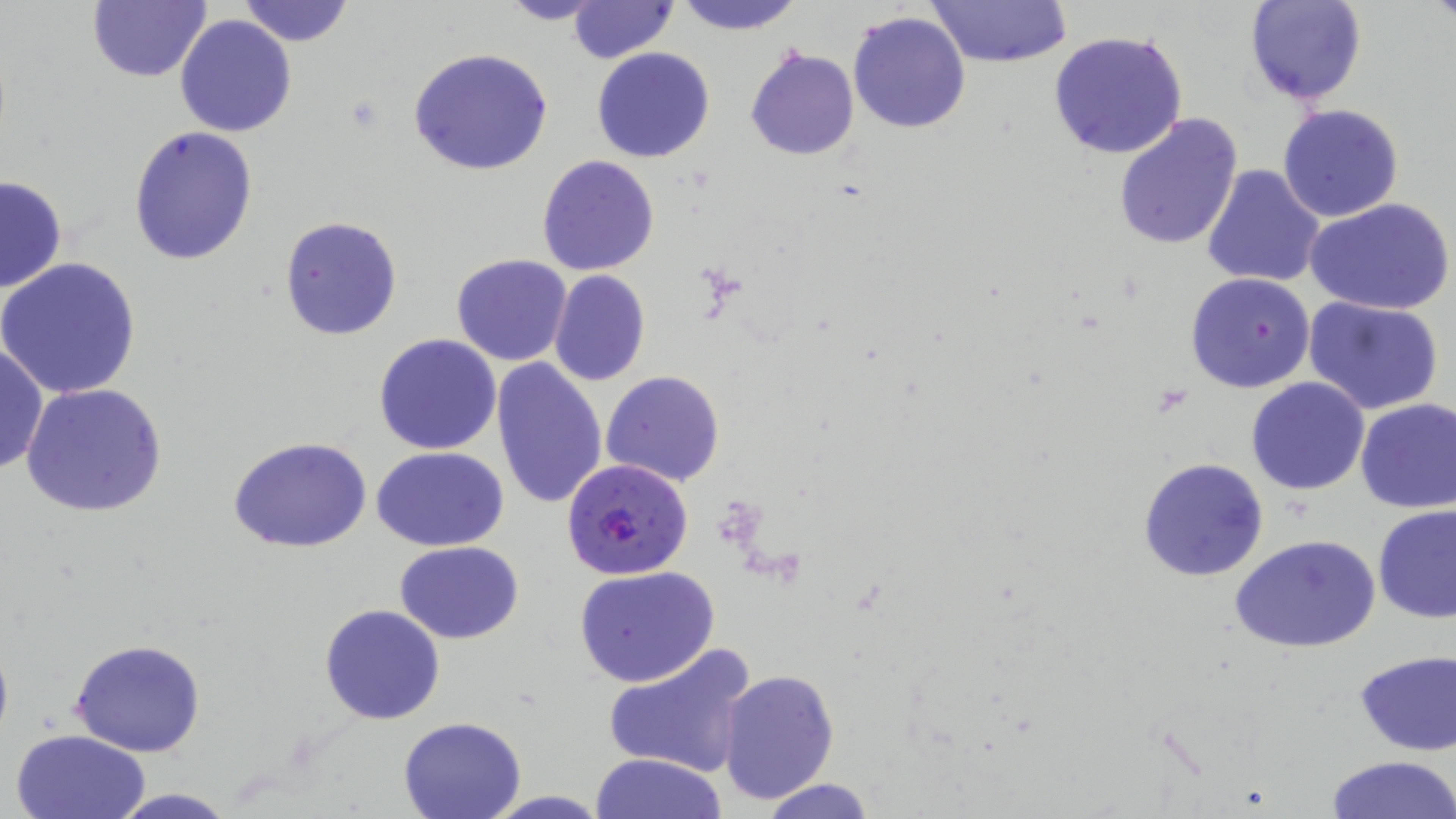

slide-level diagnosis = Plasmodium falciparum
field of view = one of a larger specimen
uninfected red blood cell locations = approximate bounding boxes as (x1,y1)-(x2,y2) corner pairs in pixels: (87,0)-(212,84), (236,0)-(356,48), (494,0)-(613,26), (670,0)-(804,35), (925,0)-(1072,69), (1244,0)-(1366,106), (570,1)-(676,61), (847,10)-(971,134), (174,14)-(298,137), (1047,29)-(1188,160), (407,47)-(553,176), (591,47)-(715,163), (745,48)-(859,161), (1277,104)-(1405,222), (1112,111)-(1242,252), (128,126)-(259,267), (537,155)-(659,276), (1201,164)-(1327,288), (0,174)-(67,295), (1306,198)-(1455,316), (278,213)-(401,341), (450,254)-(573,366), (1,258)-(142,399), (550,270)-(651,386), (1185,273)-(1315,393), (1303,296)-(1444,416), (373,334)-(503,455), (0,339)-(48,477), (492,359)-(608,512), (601,370)-(726,488), (1245,377)-(1370,495), (20,382)-(169,518), (1355,397)-(1456,513), (227,437)-(375,553), (370,445)-(510,550), (1137,456)-(1269,581), (1373,503)-(1455,624), (1229,533)-(1381,655), (395,541)-(523,643), (574,565)-(720,687), (319,604)-(445,725), (69,637)-(206,756), (602,637)-(758,780), (1353,650)-(1456,755), (717,669)-(840,805), (396,715)-(526,819), (10,728)-(151,819), (591,752)-(726,819), (1326,755)-(1456,818), (755,778)-(879,818), (104,788)-(244,819)
preparation = thin blood film
magnification = 1000x
Plasmodium falciparum-infected red blood cell locations = approximate bounding boxes as (x1,y1)-(x2,y2) corner pairs in pixels: (562,458)-(695,582)
modality = light microscopy
stain = May-Grünwald-Giemsa
image size = 1456×819 pixels